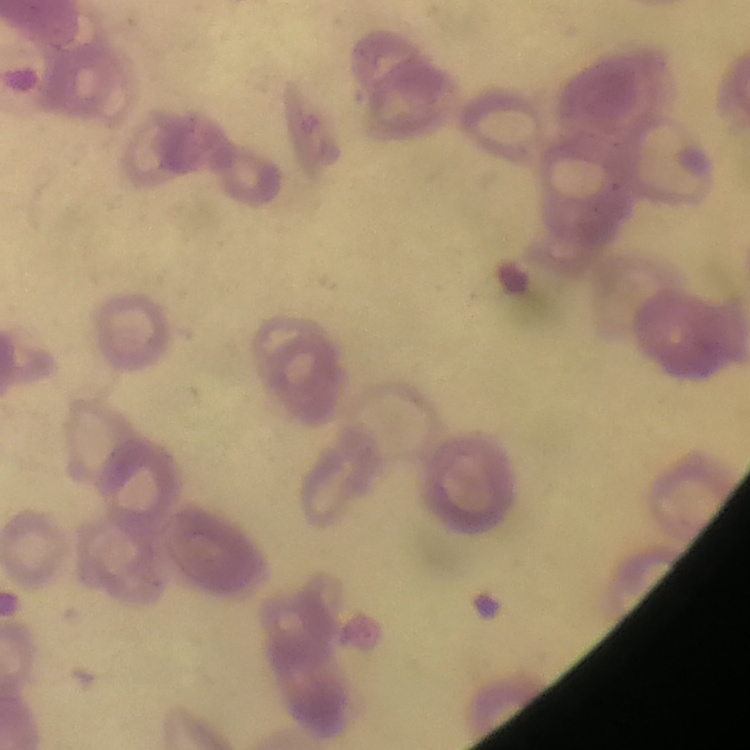

Summary:
  - Erythrocyte morphology: rouleaux formation
  - Image type: square crop of a larger photomicrograph
  - Preparation: thin blood smear
  - Stain: Field's or Giemsa